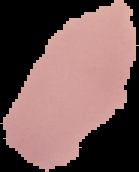

Cell region segmented out of the field of view; the surrounding area is masked to black. Malaria status: uninfected. From a thin blood film. Image is 139×172 pixels.